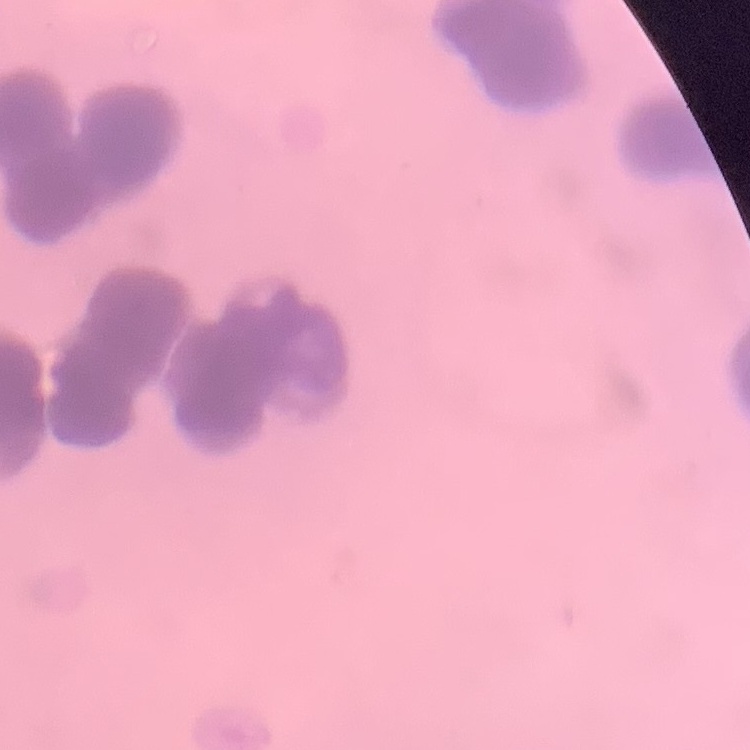

The red blood cells show rouleaux formation. Thin blood film. One tile cut from a larger photomicrograph. Stained with either Field's or Giemsa.